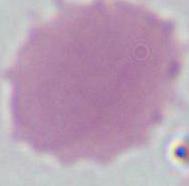
A red blood cell is shown. Photomicrograph. Captured at 1000x magnification.